Give the preparation type.
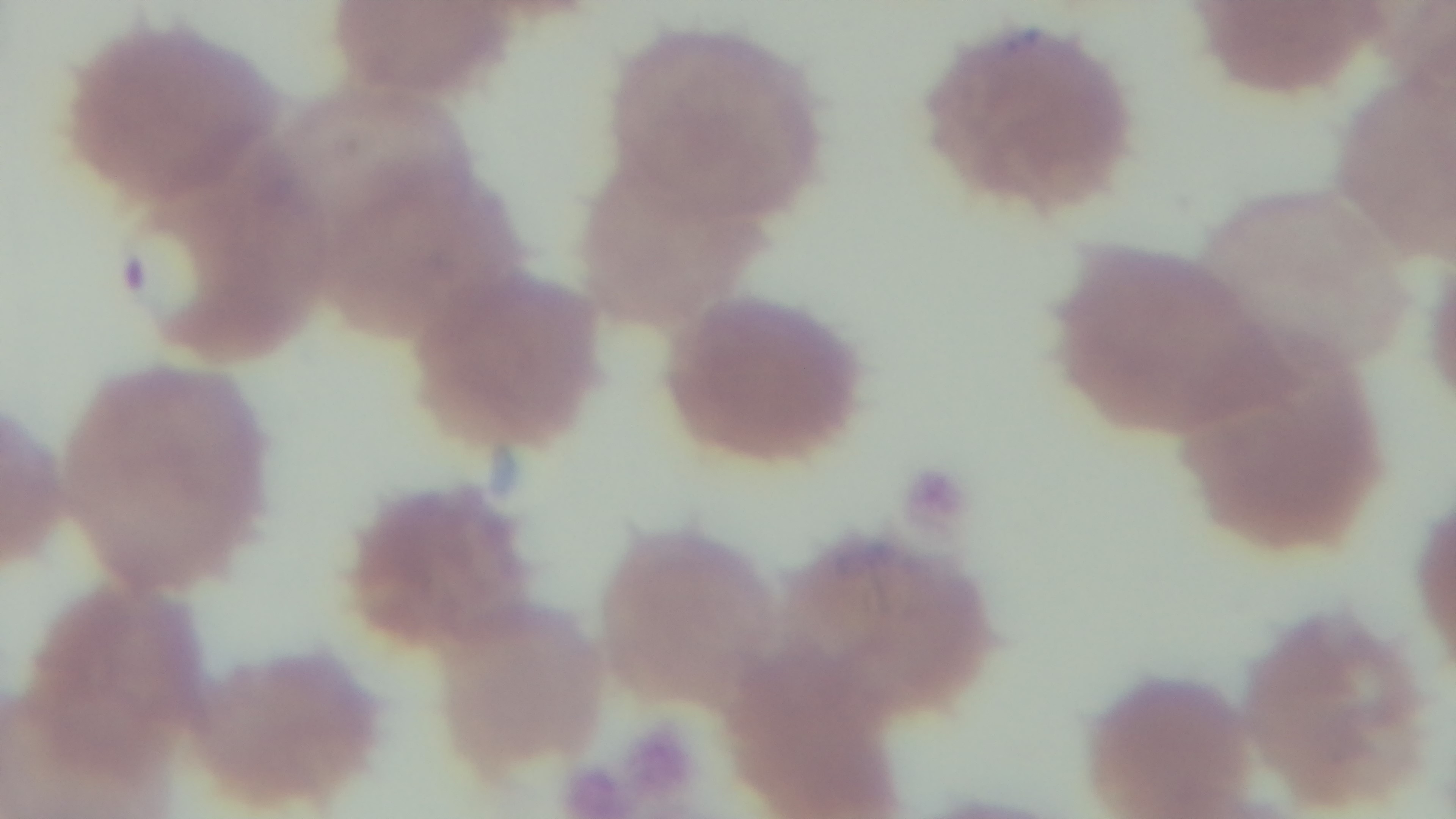

It is a thin blood film.

100x oil-immersion objective. Malaria status: positive. Captured with a mounted 4K digital camera. Giemsa-stained. Light microscopy. One field from the slide.